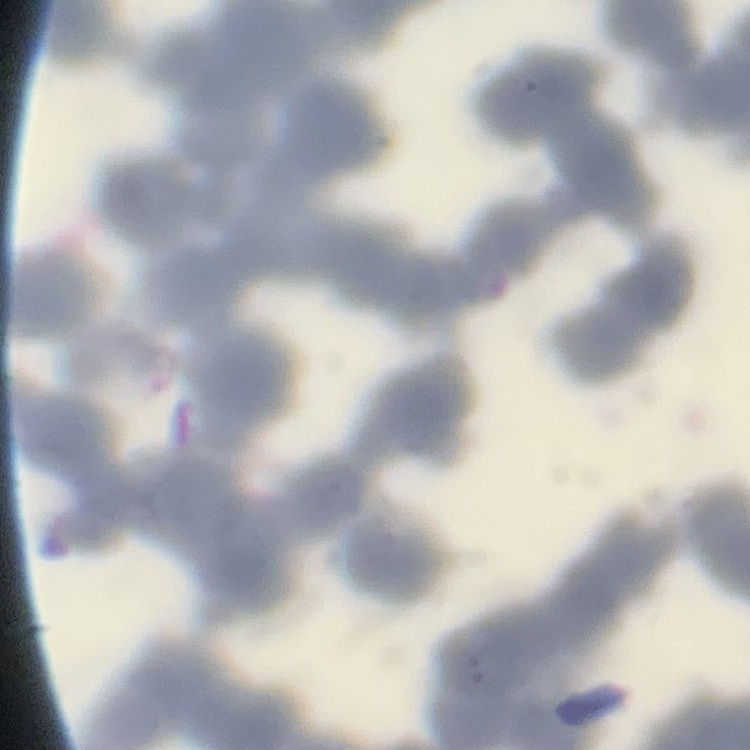
{
  "red_blood_cell_morphology": "rouleaux formation",
  "preparation": "thin blood smear",
  "image_type": "one tile cut from a larger photomicrograph",
  "stain": "Field's or Giemsa"
}